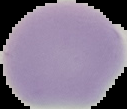

Summary:
  - Result: negative for Plasmodium parasites
  - Preparation: thin blood film
  - Image size: 127×109 pixels
  - Image type: segmented cell region on a black background